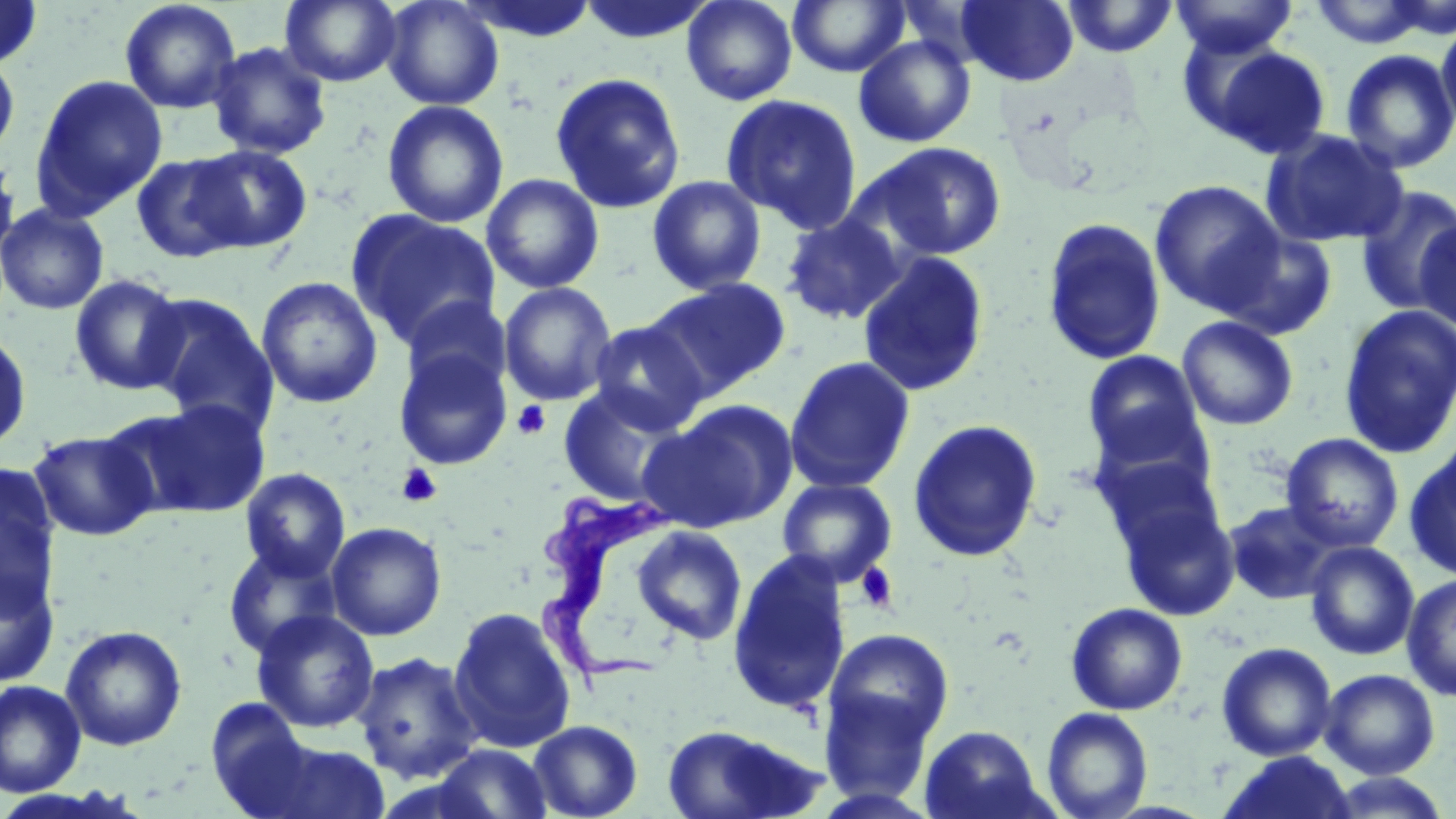

{
  "trypanosoma_brucei_locations": "approximate bounding boxes as named x1/y1/x2/y2 corners in pixels: (x1=530, y1=490, x2=680, y2=691)",
  "slide_level_diagnosis": "Trypanosoma brucei",
  "stain": "May-Grünwald-Giemsa",
  "uninfected_red_blood_cell_locations": "approximate bounding boxes as named x1/y1/x2/y2 corners in pixels: (x1=0, y1=0, x2=44, y2=70), (x1=119, y1=0, x2=242, y2=114), (x1=279, y1=0, x2=402, y2=87), (x1=380, y1=0, x2=504, y2=110), (x1=458, y1=0, x2=600, y2=43), (x1=682, y1=0, x2=798, y2=106), (x1=787, y1=0, x2=910, y2=77), (x1=956, y1=0, x2=1078, y2=86), (x1=1060, y1=0, x2=1179, y2=58), (x1=1170, y1=0, x2=1298, y2=58), (x1=577, y1=1, x2=717, y2=45), (x1=1306, y1=1, x2=1437, y2=49), (x1=1436, y1=18, x2=1456, y2=135), (x1=853, y1=36, x2=976, y2=147), (x1=207, y1=41, x2=332, y2=159), (x1=1197, y1=42, x2=1333, y2=159), (x1=1340, y1=48, x2=1456, y2=174), (x1=0, y1=52, x2=20, y2=161), (x1=549, y1=71, x2=687, y2=214), (x1=29, y1=74, x2=168, y2=220), (x1=720, y1=93, x2=863, y2=234), (x1=382, y1=100, x2=509, y2=228), (x1=1260, y1=128, x2=1408, y2=248), (x1=863, y1=142, x2=1007, y2=261), (x1=186, y1=144, x2=313, y2=253), (x1=0, y1=149, x2=21, y2=269), (x1=130, y1=152, x2=248, y2=263), (x1=481, y1=173, x2=604, y2=294), (x1=647, y1=175, x2=766, y2=296), (x1=1149, y1=179, x2=1285, y2=315), (x1=1354, y1=185, x2=1456, y2=314), (x1=0, y1=202, x2=110, y2=315), (x1=346, y1=210, x2=502, y2=350), (x1=780, y1=212, x2=907, y2=326), (x1=1041, y1=217, x2=1167, y2=365), (x1=1415, y1=218, x2=1456, y2=334), (x1=1217, y1=227, x2=1338, y2=341), (x1=857, y1=252, x2=990, y2=398), (x1=69, y1=274, x2=188, y2=396), (x1=256, y1=275, x2=384, y2=408), (x1=646, y1=277, x2=791, y2=400), (x1=498, y1=282, x2=617, y2=406), (x1=140, y1=292, x2=278, y2=432), (x1=1338, y1=304, x2=1456, y2=459), (x1=1176, y1=316, x2=1299, y2=430), (x1=587, y1=320, x2=710, y2=434), (x1=0, y1=328, x2=33, y2=455), (x1=392, y1=345, x2=513, y2=471), (x1=1082, y1=349, x2=1207, y2=466), (x1=784, y1=356, x2=915, y2=493), (x1=557, y1=384, x2=696, y2=509), (x1=126, y1=398, x2=273, y2=519), (x1=644, y1=400, x2=796, y2=532), (x1=1084, y1=409, x2=1219, y2=510), (x1=908, y1=418, x2=1043, y2=562), (x1=28, y1=429, x2=158, y2=541), (x1=1281, y1=432, x2=1404, y2=552), (x1=1405, y1=442, x2=1456, y2=581), (x1=0, y1=465, x2=62, y2=613), (x1=240, y1=468, x2=351, y2=581), (x1=776, y1=476, x2=897, y2=586), (x1=1109, y1=479, x2=1240, y2=621), (x1=1224, y1=500, x2=1343, y2=604), (x1=326, y1=521, x2=447, y2=641), (x1=631, y1=525, x2=747, y2=645), (x1=1304, y1=541, x2=1419, y2=660), (x1=223, y1=543, x2=343, y2=659), (x1=727, y1=549, x2=853, y2=716), (x1=0, y1=566, x2=59, y2=687), (x1=1402, y1=573, x2=1456, y2=703), (x1=1065, y1=601, x2=1188, y2=715), (x1=446, y1=605, x2=578, y2=753), (x1=251, y1=609, x2=380, y2=733), (x1=60, y1=625, x2=187, y2=751), (x1=822, y1=627, x2=955, y2=755), (x1=1216, y1=642, x2=1337, y2=761), (x1=352, y1=651, x2=482, y2=784), (x1=1319, y1=668, x2=1440, y2=779), (x1=0, y1=680, x2=86, y2=797), (x1=818, y1=685, x2=939, y2=806), (x1=1041, y1=707, x2=1153, y2=819), (x1=527, y1=719, x2=644, y2=819), (x1=660, y1=722, x2=826, y2=819), (x1=919, y1=725, x2=1046, y2=818), (x1=260, y1=738, x2=393, y2=819), (x1=430, y1=743, x2=554, y2=818), (x1=1218, y1=751, x2=1357, y2=819), (x1=1321, y1=772, x2=1452, y2=818)",
  "image_size": "1456×819 pixels",
  "magnification": "1000x",
  "preparation": "thin blood smear",
  "platelet_locations": "approximate bounding boxes as named x1/y1/x2/y2 corners in pixels: (x1=512, y1=400, x2=552, y2=440), (x1=397, y1=463, x2=442, y2=507), (x1=855, y1=563, x2=899, y2=613)",
  "field_of_view": "one of a larger specimen",
  "modality": "light microscopy"
}